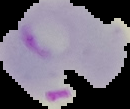

Image is 130×109 pixels. Segmented cell region on a black background. From a thin blood film. Result: malaria parasites identified.